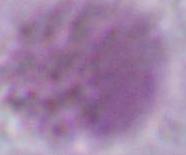 1000x magnification. An erythrocyte is seen. Photomicrograph.